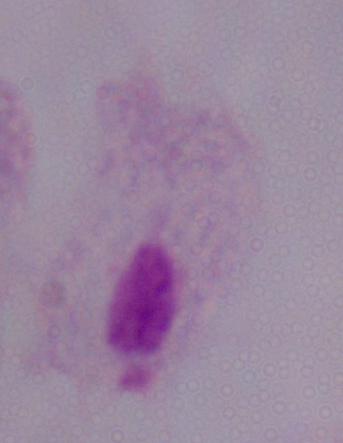
identification = trichomonad
modality = photomicrograph
magnification = 1000x